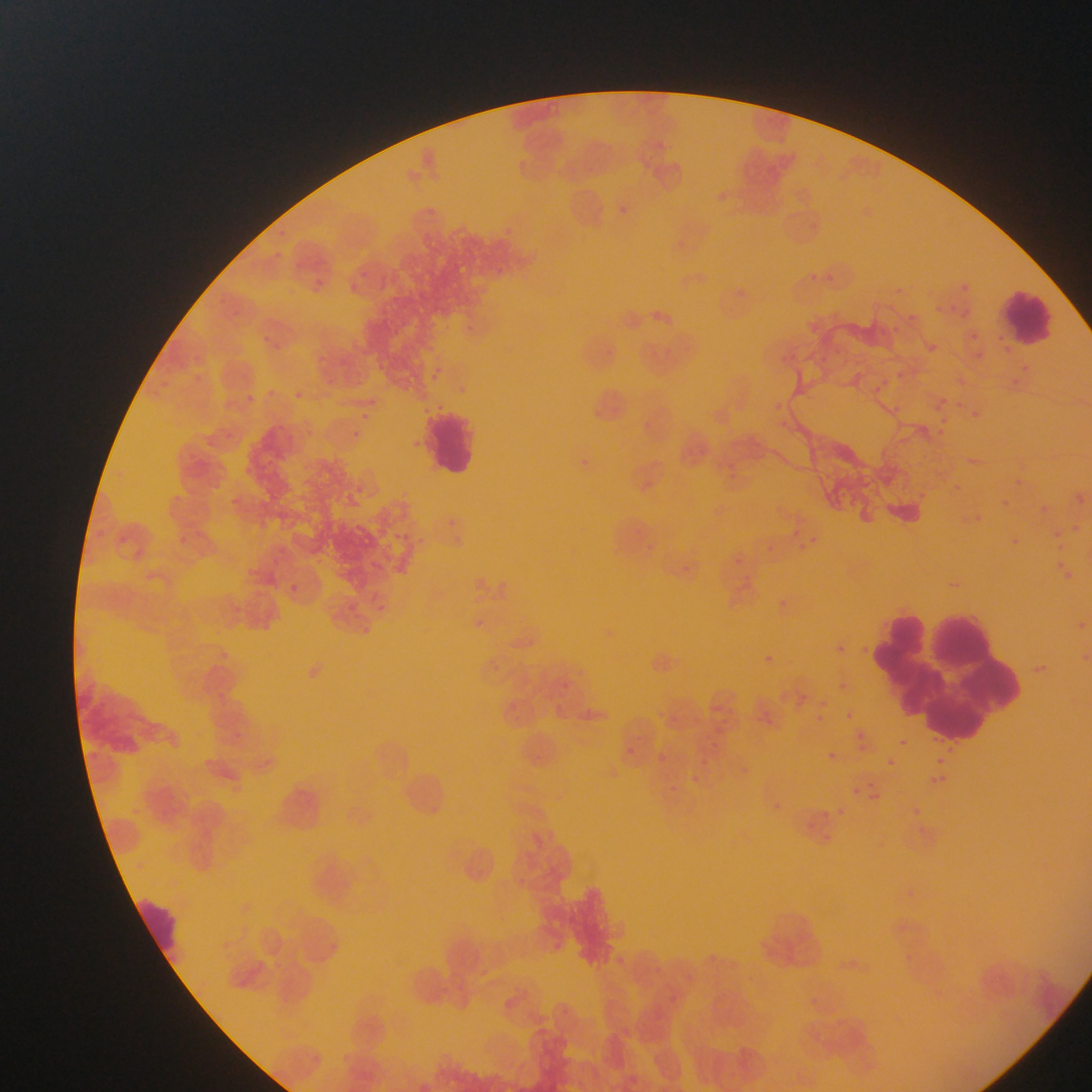
Approximate bounding boxes as left top right bottom in pixels. Leukocyte locations: 1000 285 1057 352; 426 407 476 479; 863 589 1019 735; 138 894 184 972. Malaria parasite locations: 615 202 642 229; 508 225 528 249; 259 249 282 264; 358 264 376 284; 496 264 521 290; 816 266 838 286; 317 276 336 302; 955 277 973 297; 350 282 369 300; 740 288 768 311; 907 302 918 322; 949 302 973 317; 654 303 685 333; 258 325 280 355; 888 325 908 343; 965 330 979 347; 925 333 941 365; 818 351 837 373; 1017 360 1034 374; 430 367 454 380; 894 368 910 382; 189 370 213 389; 1009 376 1024 396; 866 379 890 400; 263 382 286 402; 230 392 257 411; 293 393 311 411; 933 394 951 414; 766 395 784 416; 948 395 984 422; 882 402 909 420; 356 407 372 426; 937 415 951 428; 934 426 954 452; 345 429 371 449; 407 438 422 452; 717 458 739 478; 239 462 266 482; 947 482 969 500; 1076 487 1092 512; 221 491 248 510; 994 491 1013 510; 1041 501 1067 516; 956 510 984 538; 169 514 192 548; 441 514 464 542; 1048 522 1067 541; 1004 524 1021 561; 791 528 814 549; 119 538 127 545; 638 538 654 554; 761 542 776 555; 737 554 748 572; 1053 555 1077 582; 367 558 386 571; 667 560 693 577; 742 576 757 586; 287 580 300 590; 775 594 790 616; 376 604 393 617; 474 614 488 635; 1083 622 1092 631; 357 623 379 636; 834 638 848 652; 1073 642 1092 668; 753 649 779 666; 490 656 507 677; 1032 657 1059 670; 837 677 854 693; 558 678 572 693; 816 692 829 712; 814 711 827 723; 845 711 853 720; 708 712 739 730; 658 716 674 729; 229 724 261 754; 856 729 865 737; 706 731 720 747; 934 734 964 753; 898 739 908 747; 855 740 870 761; 623 743 641 759; 827 751 836 760; 659 752 669 766; 698 754 713 768; 198 756 221 772; 740 758 754 780; 886 758 895 766; 936 758 944 766; 688 769 705 789; 930 774 958 783; 929 776 937 784; 842 780 869 799; 664 782 686 804; 868 785 891 804; 772 799 785 813; 815 801 831 824; 911 804 926 820; 833 807 852 818; 803 815 820 837; 909 825 937 836; 819 830 837 845; 548 937 568 960; 616 947 632 975; 649 966 666 982; 667 996 685 1016. Photographed through a microscope with a mobile-phone camera. Image is 1092×1092 pixels. One field of view. Thin blood smear. Sample from Ghana.